Outline each uninfected red blood cell.
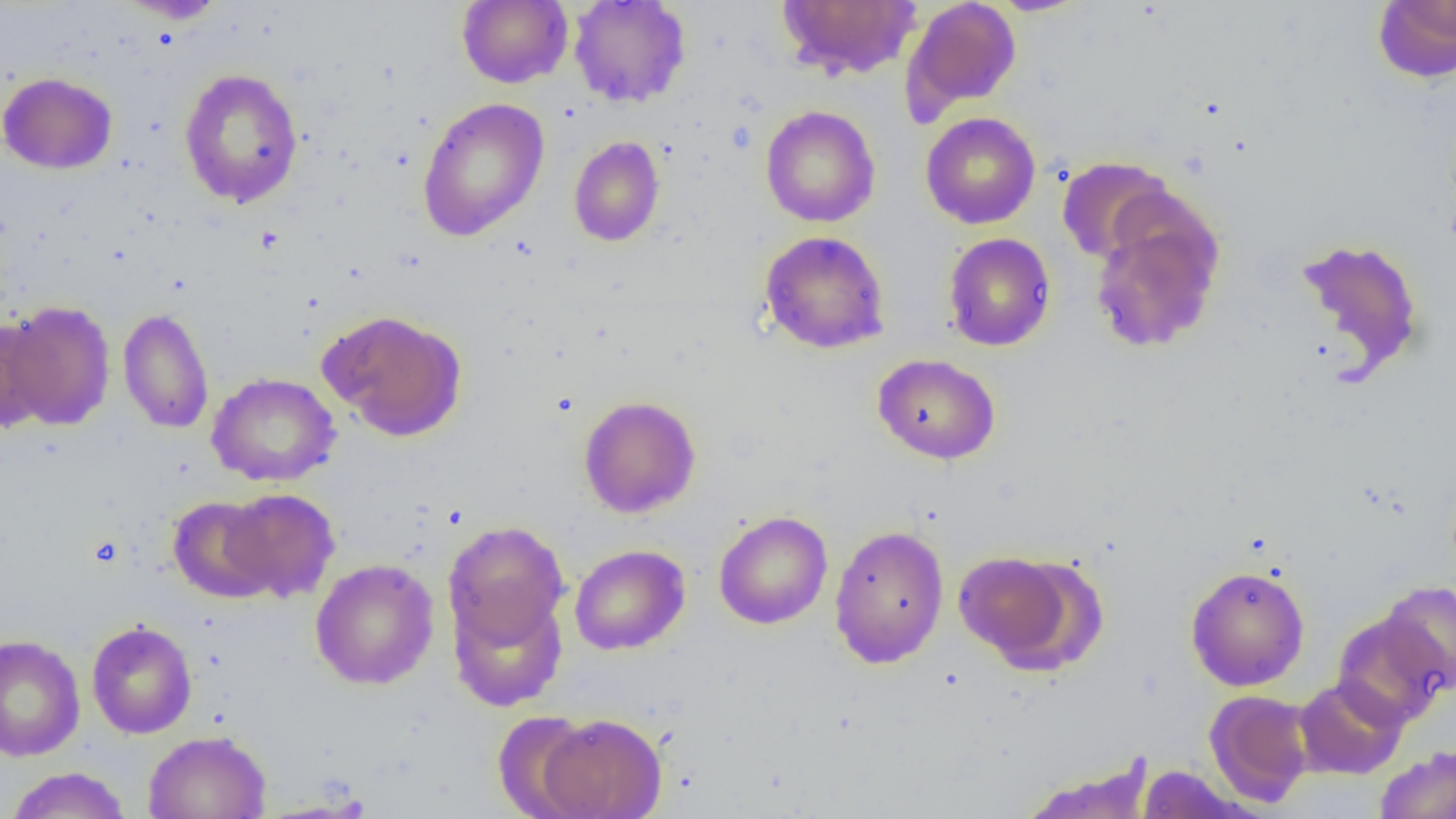
Approximate bounding boxes as [x1, y1, x2, y2] in pixels.
Uninfected red blood cells: [115, 0, 227, 23], [457, 0, 573, 89], [568, 0, 691, 108], [776, 0, 922, 81], [901, 0, 1022, 120], [986, 0, 1094, 16], [1372, 1, 1456, 84], [178, 67, 304, 209], [0, 71, 117, 174], [416, 97, 550, 241], [760, 105, 881, 228], [920, 112, 1040, 229], [569, 136, 665, 247], [1056, 156, 1177, 266], [1089, 211, 1223, 353], [759, 230, 890, 354], [943, 232, 1056, 351], [1294, 237, 1425, 379], [2, 300, 116, 432], [118, 307, 215, 434], [318, 309, 468, 442], [0, 316, 50, 433], [873, 353, 1000, 464], [207, 372, 341, 487], [578, 395, 701, 518], [221, 487, 341, 602], [167, 496, 280, 602], [713, 511, 833, 629], [443, 521, 569, 651], [829, 524, 949, 669], [569, 544, 690, 655], [953, 549, 1090, 671], [310, 558, 439, 690], [1185, 565, 1310, 691], [1379, 581, 1456, 693], [448, 587, 568, 711], [1332, 610, 1451, 728], [86, 620, 197, 739], [0, 634, 85, 762], [1293, 675, 1408, 779], [1204, 689, 1315, 807], [493, 710, 597, 819], [536, 712, 667, 819], [143, 730, 271, 819], [1375, 746, 1456, 819], [1016, 757, 1156, 819], [1136, 764, 1250, 818], [4, 767, 132, 819].

Summary:
  - Slide-level diagnosis: negative for blood parasites
  - Modality: optical microscopy
  - Magnification: 1000x
  - Field of view: single
  - Image size: 1456×819 pixels
  - Preparation: thin blood smear